Outline each Plasmodium falciparum-infected red blood cell.
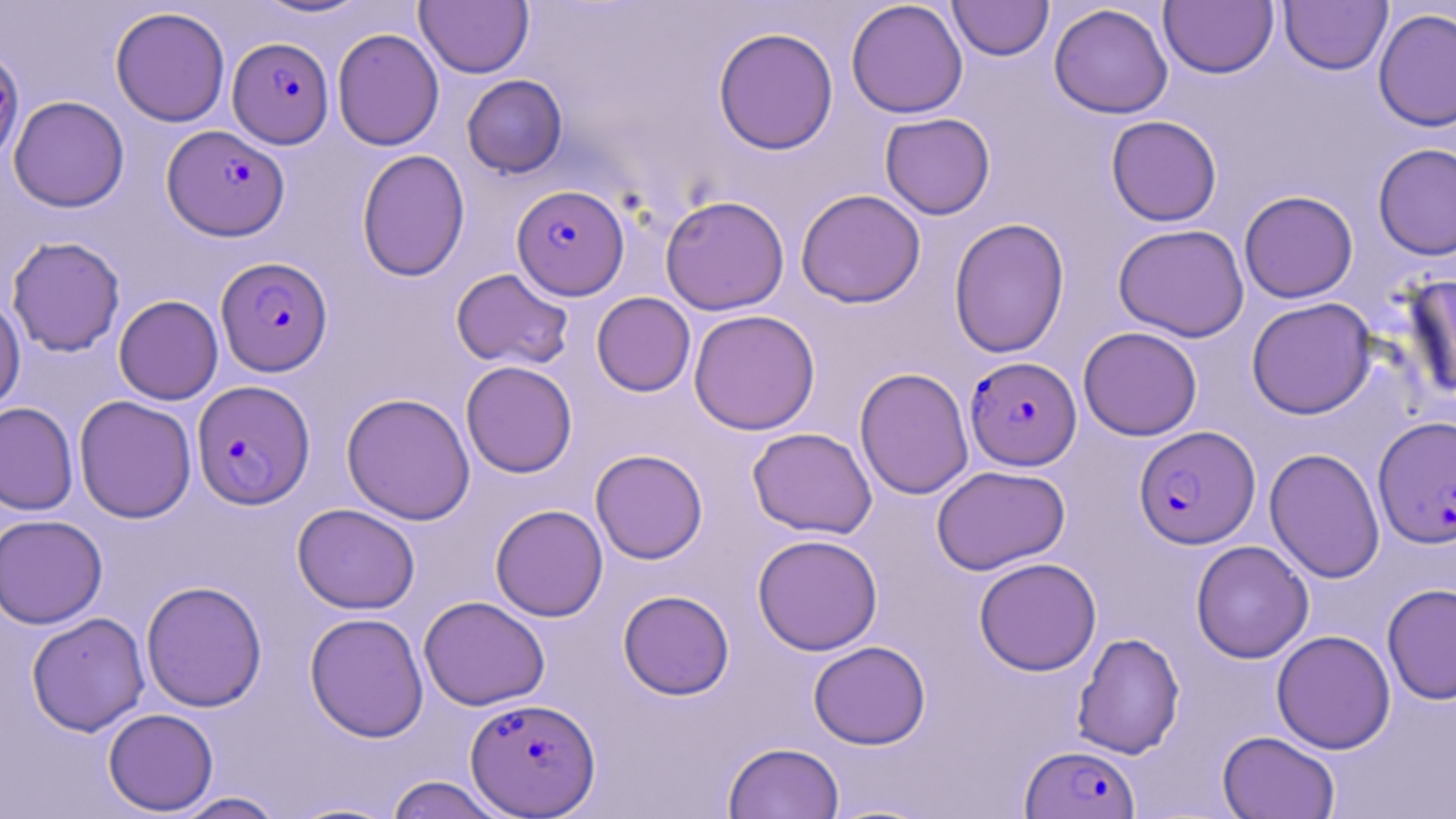
Approximate bounding boxes as named x1/y1/x2/y2 corners in pixels.
Plasmodium falciparum-infected red blood cells: (x1=228, y1=37, x2=333, y2=148), (x1=162, y1=125, x2=290, y2=241), (x1=511, y1=184, x2=630, y2=300), (x1=215, y1=257, x2=332, y2=375), (x1=965, y1=356, x2=1081, y2=470), (x1=192, y1=379, x2=315, y2=509), (x1=1373, y1=416, x2=1456, y2=549), (x1=1134, y1=426, x2=1260, y2=548), (x1=464, y1=697, x2=600, y2=816), (x1=1021, y1=744, x2=1140, y2=819).

slide-level diagnosis = Plasmodium falciparum
preparation = thin blood smear
uninfected red blood cell locations = approximate bounding boxes as named x1/y1/x2/y2 corners in pixels: (x1=252, y1=0, x2=374, y2=19), (x1=845, y1=0, x2=968, y2=119), (x1=415, y1=1, x2=534, y2=78), (x1=948, y1=1, x2=1053, y2=61), (x1=1159, y1=1, x2=1278, y2=78), (x1=1280, y1=1, x2=1392, y2=75), (x1=1049, y1=3, x2=1173, y2=119), (x1=110, y1=6, x2=230, y2=127), (x1=1373, y1=7, x2=1456, y2=133), (x1=713, y1=26, x2=839, y2=155), (x1=332, y1=27, x2=444, y2=151), (x1=0, y1=45, x2=25, y2=166), (x1=462, y1=75, x2=567, y2=177), (x1=8, y1=95, x2=130, y2=212), (x1=880, y1=113, x2=995, y2=219), (x1=1106, y1=115, x2=1222, y2=226), (x1=1372, y1=142, x2=1456, y2=261), (x1=356, y1=149, x2=470, y2=282), (x1=796, y1=189, x2=926, y2=308), (x1=1238, y1=190, x2=1358, y2=303), (x1=660, y1=195, x2=789, y2=315), (x1=948, y1=217, x2=1070, y2=358), (x1=1113, y1=223, x2=1250, y2=342), (x1=6, y1=236, x2=125, y2=357), (x1=450, y1=268, x2=575, y2=370), (x1=1400, y1=274, x2=1456, y2=402), (x1=591, y1=292, x2=695, y2=396), (x1=0, y1=294, x2=25, y2=415), (x1=114, y1=295, x2=223, y2=405), (x1=1246, y1=297, x2=1376, y2=419), (x1=688, y1=309, x2=820, y2=435), (x1=1078, y1=326, x2=1202, y2=441), (x1=460, y1=361, x2=578, y2=478), (x1=854, y1=367, x2=974, y2=500), (x1=341, y1=392, x2=475, y2=524), (x1=74, y1=395, x2=197, y2=523), (x1=0, y1=402, x2=79, y2=515), (x1=747, y1=427, x2=877, y2=538), (x1=1264, y1=447, x2=1385, y2=583), (x1=590, y1=449, x2=708, y2=564), (x1=931, y1=464, x2=1070, y2=575), (x1=292, y1=503, x2=420, y2=614), (x1=490, y1=504, x2=608, y2=622), (x1=0, y1=514, x2=108, y2=629), (x1=752, y1=533, x2=883, y2=655), (x1=1190, y1=540, x2=1314, y2=663), (x1=974, y1=557, x2=1102, y2=676), (x1=141, y1=580, x2=267, y2=712), (x1=1382, y1=583, x2=1456, y2=704), (x1=618, y1=589, x2=734, y2=699), (x1=419, y1=595, x2=550, y2=711), (x1=26, y1=612, x2=150, y2=736), (x1=304, y1=612, x2=429, y2=742), (x1=1271, y1=630, x2=1396, y2=754), (x1=1072, y1=632, x2=1185, y2=759), (x1=808, y1=640, x2=931, y2=749), (x1=102, y1=708, x2=219, y2=815), (x1=1217, y1=730, x2=1340, y2=819), (x1=723, y1=742, x2=845, y2=819), (x1=384, y1=775, x2=509, y2=819), (x1=170, y1=791, x2=287, y2=819), (x1=283, y1=799, x2=402, y2=818)
stain = May-Grünwald-Giemsa
image size = 1456×819 pixels
modality = light microscopy
magnification = 1000x
field of view = single